Identify the blood parasite species.
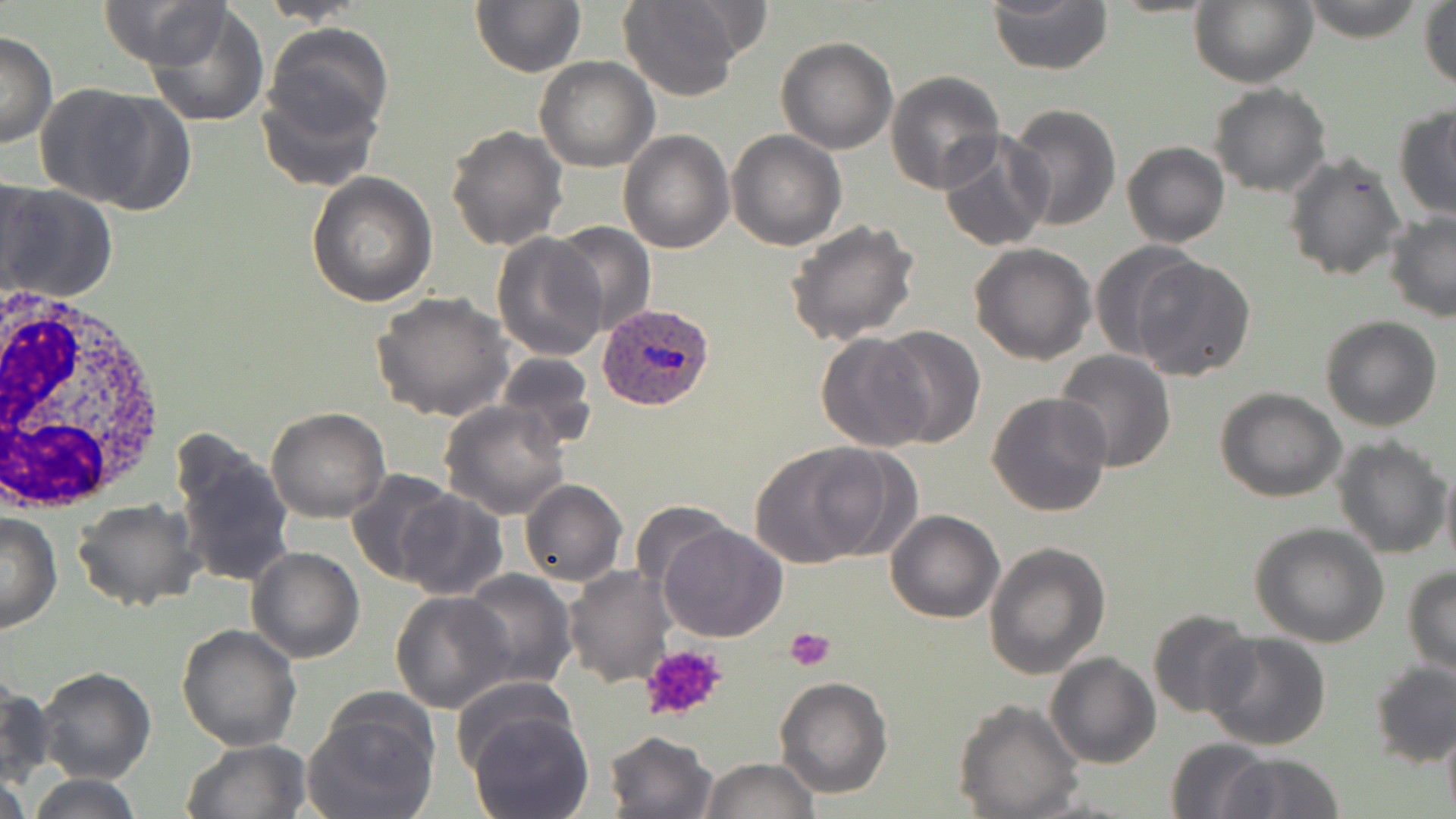
Plasmodium ovale.

preparation = thin blood smear
Plasmodium ovale-infected red blood cell locations = approximate bounding boxes as (x1,y1)-(x2,y2) corner pairs in pixels: (594,303)-(716,413)
magnification = 1000x
uninfected red blood cell locations = approximate bounding boxes as (x1,y1)-(x2,y2) corner pairs in pixels: (99,0)-(225,70), (469,0)-(585,77), (987,0)-(1112,74), (1299,0)-(1425,43), (257,1)-(374,25), (617,1)-(746,101), (1189,2)-(1318,87), (1419,2)-(1456,91), (144,3)-(271,128), (264,24)-(393,146), (0,31)-(57,149), (775,37)-(898,154), (534,57)-(658,172), (883,70)-(1005,194), (255,77)-(382,193), (1209,83)-(1332,198), (34,84)-(188,215), (1005,104)-(1121,231), (1393,106)-(1456,222), (444,124)-(567,250), (618,130)-(734,253), (727,130)-(846,251), (938,131)-(1052,251), (1121,142)-(1230,248), (1283,149)-(1407,283), (306,172)-(436,307), (1,175)-(46,297), (3,183)-(119,305), (1384,212)-(1456,322), (786,218)-(921,346), (549,220)-(656,337), (491,232)-(609,361), (1088,240)-(1203,362), (969,243)-(1096,365), (1132,255)-(1256,380), (371,292)-(514,425), (1320,314)-(1445,431), (873,327)-(985,447), (817,333)-(931,453), (1055,350)-(1177,472), (494,353)-(599,448), (1215,386)-(1346,501), (986,392)-(1114,518), (438,401)-(572,520), (266,407)-(389,522), (1332,435)-(1451,557), (172,440)-(296,592), (750,441)-(897,567), (1440,458)-(1456,572), (346,469)-(461,587), (518,479)-(627,587), (394,490)-(510,600), (72,498)-(202,613), (631,500)-(736,595), (884,510)-(1004,624), (1,511)-(61,632), (657,522)-(787,643), (1249,523)-(1390,647), (985,542)-(1112,682), (246,546)-(364,663), (563,565)-(674,687), (1403,567)-(1455,676), (458,569)-(577,690), (390,592)-(515,712), (1147,609)-(1257,716), (177,622)-(303,751), (1201,632)-(1331,752), (1046,652)-(1159,768), (1368,660)-(1456,768), (34,667)-(157,784), (967,669)-(1157,792), (773,676)-(893,800), (0,680)-(52,792), (450,680)-(577,776), (303,695)-(438,819), (953,699)-(1084,818), (466,710)-(594,819), (1440,719)-(1456,819), (604,729)-(718,818), (1166,737)-(1273,818), (181,740)-(309,819), (1221,751)-(1345,818), (700,757)-(820,817), (0,771)-(30,819), (25,773)-(146,819)
platelet locations = approximate bounding boxes as (x1,y1)-(x2,y2) corner pairs in pixels: (784,628)-(836,672), (639,642)-(728,724)
stain = May-Grünwald-Giemsa
image size = 1456×819 pixels
modality = optical microscopy
field of view = single
white blood cell locations = approximate bounding boxes as (x1,y1)-(x2,y2) corner pairs in pixels: (3,280)-(169,513)